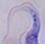
Summary:
  - Magnification: 1000x
  - Modality: photomicrograph
  - Identification: trypanosome